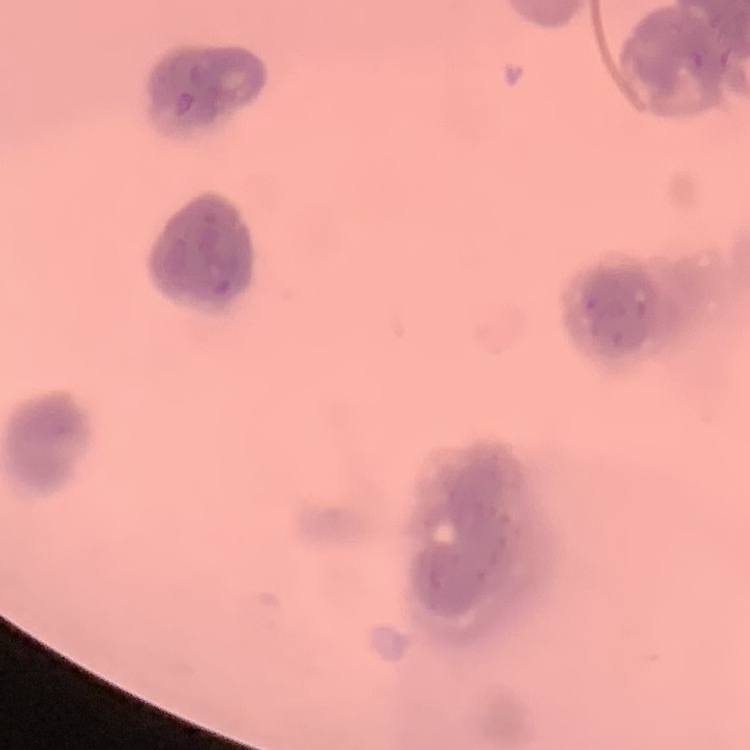
erythrocyte_morphology: rouleaux formation
stain: Field's or Giemsa
image_type: square crop of a larger photomicrograph
preparation: thin blood smear